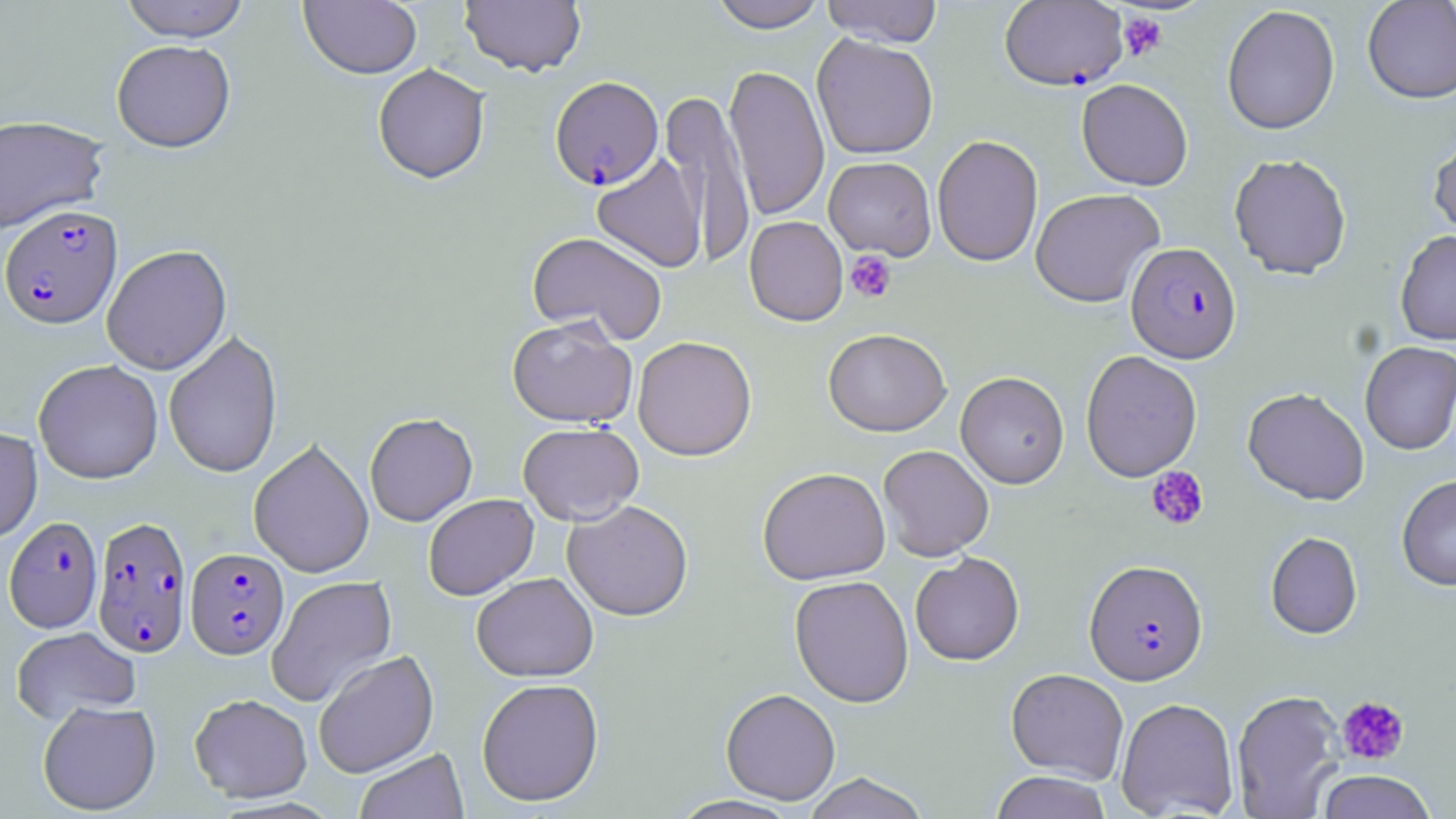

Approximate bounding boxes as (x1,y1)-(x2,y2) corner pairs in pixels. Plasmodium falciparum-infected red blood cell locations: (999,1)-(1128,91), (550,76)-(663,190), (0,204)-(122,329), (1126,242)-(1241,363), (92,515)-(192,657), (4,516)-(103,632), (185,547)-(289,659), (1084,559)-(1208,686). Uninfected red blood cell locations: (118,0)-(250,42), (707,0)-(828,32), (820,0)-(944,47), (1362,0)-(1456,104), (300,1)-(422,79), (459,1)-(586,77), (1222,5)-(1340,135), (812,34)-(938,160), (111,39)-(236,152), (373,63)-(490,184), (723,64)-(829,221), (1076,79)-(1193,190), (661,87)-(757,268), (0,114)-(109,234), (1428,131)-(1456,243), (932,135)-(1044,266), (591,152)-(707,273), (1229,153)-(1352,279), (823,156)-(936,260), (1030,188)-(1165,307), (744,216)-(848,326), (1395,230)-(1456,345), (527,231)-(668,344), (102,244)-(232,375), (507,316)-(637,428), (823,328)-(951,436), (163,330)-(283,479), (632,335)-(757,461), (1360,340)-(1456,454), (1080,350)-(1202,481), (33,359)-(163,484), (955,371)-(1069,488), (1242,387)-(1369,505), (364,412)-(477,526), (517,422)-(643,525), (0,426)-(42,544), (249,438)-(374,578), (878,445)-(994,561), (757,466)-(890,584), (1396,474)-(1456,591), (423,493)-(539,600), (562,500)-(693,621), (1265,531)-(1363,639), (910,552)-(1024,665), (471,572)-(598,682), (266,575)-(397,708), (789,575)-(914,708), (11,626)-(140,724), (313,649)-(438,778), (1006,668)-(1129,783), (476,677)-(604,806), (720,687)-(841,804), (1232,689)-(1345,818), (189,693)-(312,802), (1116,697)-(1239,818), (37,699)-(162,815), (355,747)-(469,818), (1316,770)-(1437,819), (990,771)-(1112,819), (802,772)-(931,819), (667,795)-(803,818). Platelet locations: (1118,12)-(1167,61), (845,250)-(896,303), (1146,465)-(1209,531), (1336,695)-(1410,766). Slide-level diagnosis: Plasmodium falciparum. Optical microscopy. May-Grünwald-Giemsa-stained preparation. 1000x magnification. Image is 1456×819 pixels. Thin blood film. One field of a larger specimen.